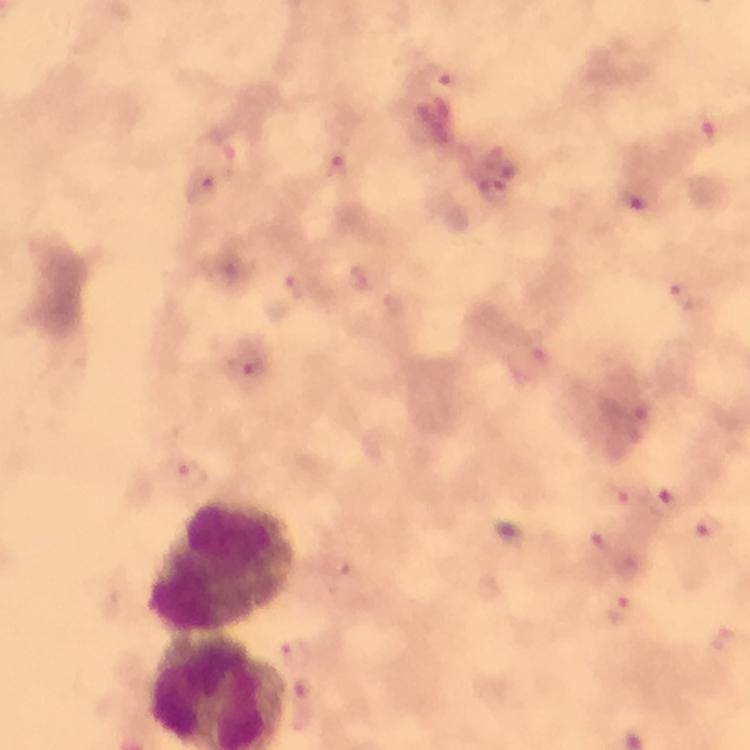 Approximate centers as [x, y] in pixels. Plasmodium parasite locations: [446, 78], [712, 121], [233, 149], [337, 169], [639, 199], [295, 289], [688, 297], [395, 307], [535, 350], [248, 365], [190, 470], [619, 497], [663, 502], [710, 527], [605, 541], [618, 611], [721, 640]. Leukocyte locations: [223, 565]. Image is 750×750 pixels. At 100x magnification. Immersion oil applied. Cropped region of a single field of view. Thick smear. Smartphone photograph taken through a microscope. From a malaria diagnostic workup. Giemsa-stained preparation.